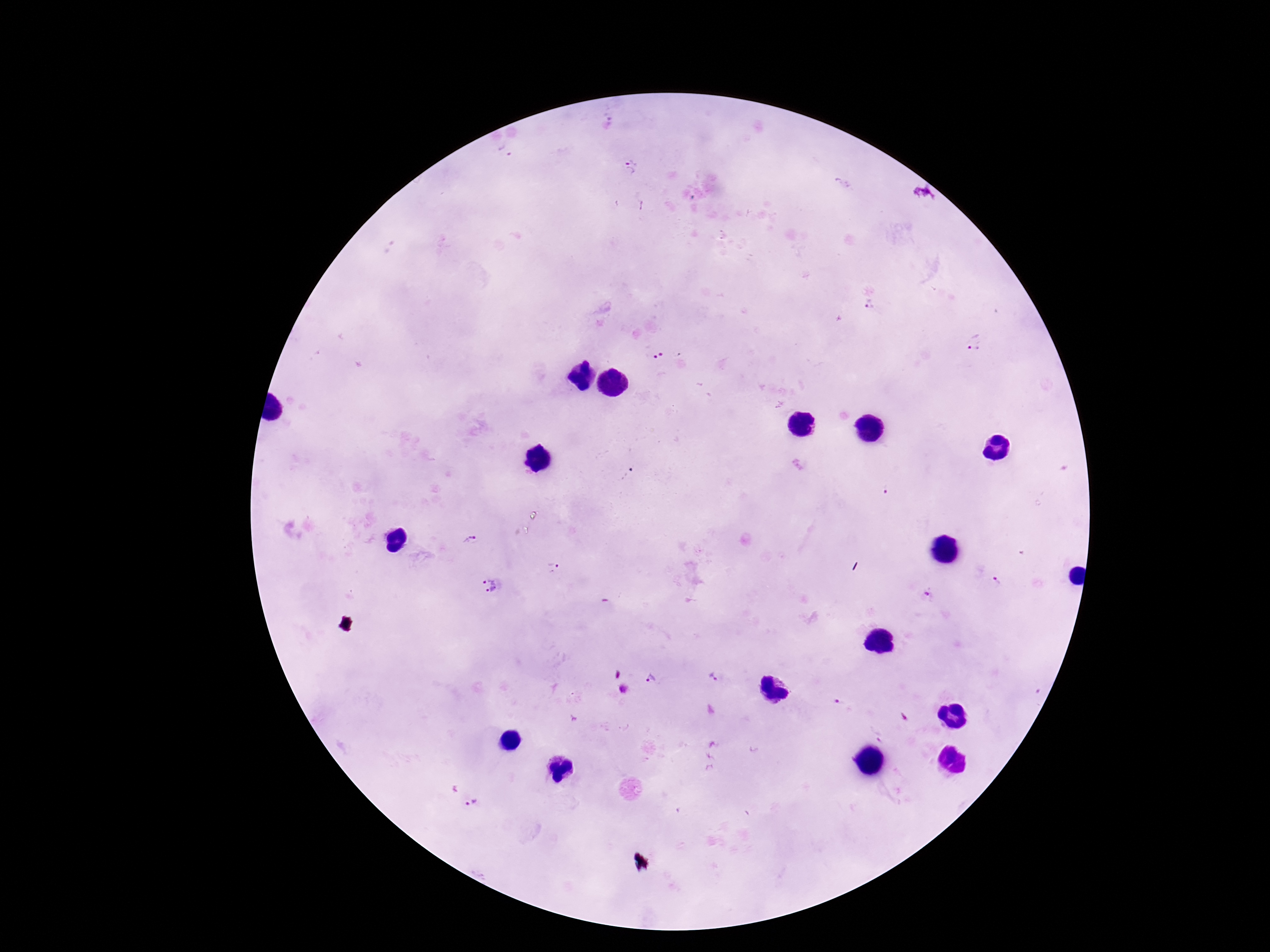
Approximate object centers, in pixels from the top-left corner.
Summary:
  - Plasmodium parasite locations: (x=503, y=152), (x=632, y=166), (x=872, y=308), (x=975, y=341), (x=658, y=356), (x=626, y=474), (x=470, y=541), (x=552, y=567), (x=995, y=578), (x=491, y=585), (x=926, y=594), (x=713, y=676), (x=652, y=680), (x=624, y=690), (x=472, y=804)
  - Preparation: thick blood film
  - Stain: Giemsa
  - Capture: smartphone camera through the microscope eyepiece
  - Magnification: 100x
  - Field of view: single
  - Patient malaria status: positive
  - Image size: 1270×952 pixels